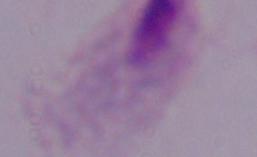
Summary:
  - Identification: trichomonad
  - Modality: photomicrograph
  - Magnification: 1000x